Locate and identify every blood parasite.
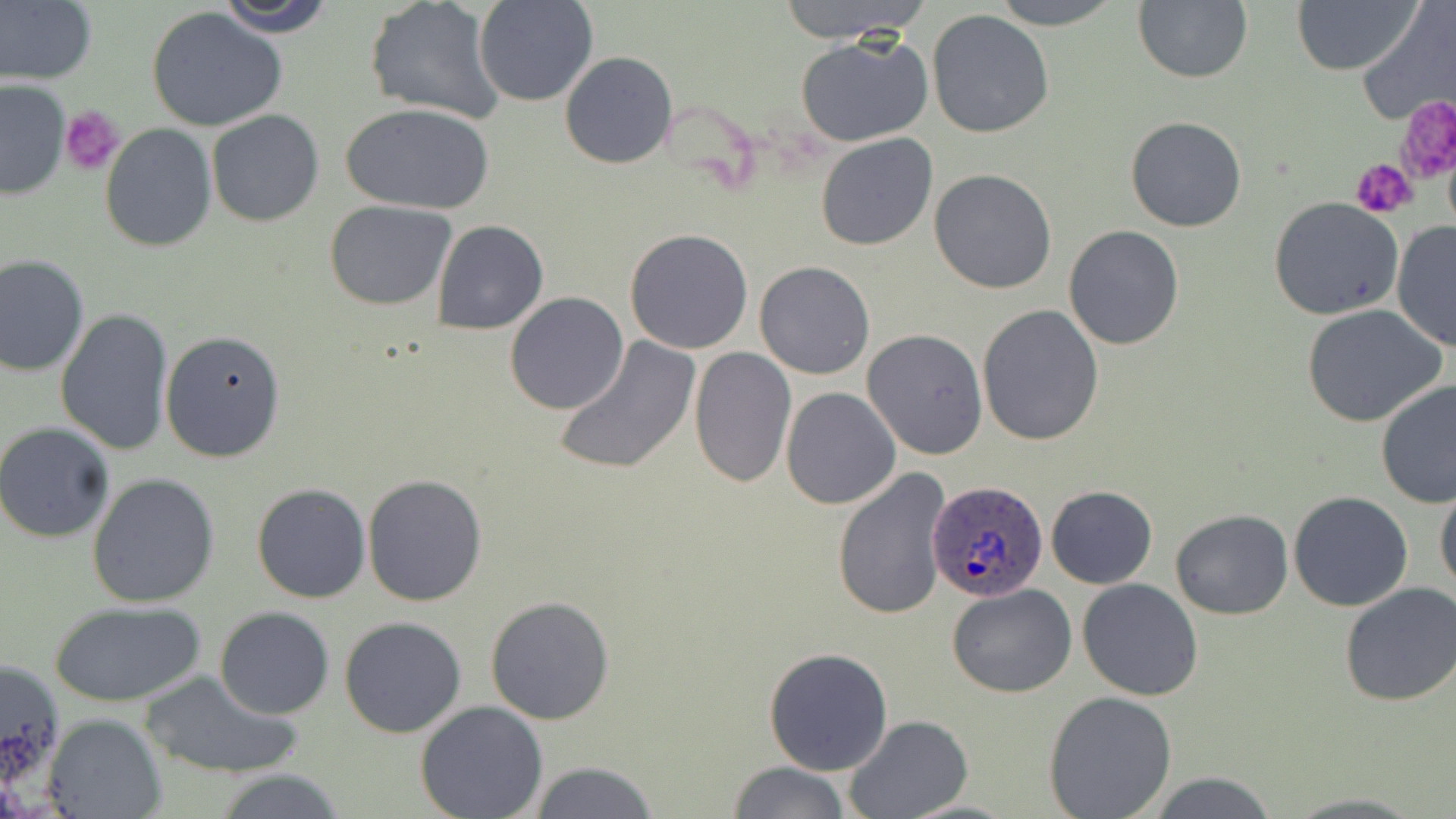

Approximate bounding boxes as named x1/y1/x2/y2 corners in pixels.
Plasmodium ovale-infected red blood cells: (x1=927, y1=479, x2=1051, y2=604).
No Plasmodium falciparum, Plasmodium malariae, Plasmodium vivax, Babesia divergens, or Trypanosoma brucei observed.

Platelet locations: (x1=1397, y1=96, x2=1456, y2=186), (x1=60, y1=106, x2=125, y2=176), (x1=1353, y1=159, x2=1416, y2=219). Uninfected red blood cell locations: (x1=215, y1=0, x2=338, y2=37), (x1=473, y1=0, x2=598, y2=106), (x1=774, y1=0, x2=929, y2=43), (x1=988, y1=0, x2=1125, y2=29), (x1=1134, y1=0, x2=1253, y2=84), (x1=1293, y1=0, x2=1417, y2=75), (x1=365, y1=1, x2=507, y2=126), (x1=0, y1=2, x2=96, y2=84), (x1=1356, y1=2, x2=1456, y2=128), (x1=147, y1=7, x2=289, y2=133), (x1=927, y1=9, x2=1055, y2=138), (x1=796, y1=36, x2=933, y2=147), (x1=560, y1=52, x2=677, y2=170), (x1=0, y1=80, x2=71, y2=199), (x1=340, y1=101, x2=495, y2=215), (x1=206, y1=110, x2=324, y2=227), (x1=1124, y1=115, x2=1247, y2=232), (x1=100, y1=124, x2=217, y2=251), (x1=815, y1=132, x2=938, y2=250), (x1=929, y1=170, x2=1058, y2=294), (x1=1267, y1=197, x2=1405, y2=319), (x1=324, y1=199, x2=457, y2=311), (x1=1392, y1=218, x2=1456, y2=352), (x1=430, y1=220, x2=548, y2=336), (x1=1063, y1=225, x2=1183, y2=351), (x1=624, y1=228, x2=754, y2=355), (x1=0, y1=253, x2=90, y2=376), (x1=754, y1=261, x2=876, y2=380), (x1=505, y1=292, x2=628, y2=414), (x1=977, y1=303, x2=1105, y2=446), (x1=1301, y1=303, x2=1447, y2=427), (x1=55, y1=307, x2=173, y2=457), (x1=159, y1=329, x2=286, y2=462), (x1=863, y1=329, x2=989, y2=458), (x1=553, y1=337, x2=701, y2=477), (x1=688, y1=346, x2=796, y2=489), (x1=1376, y1=379, x2=1456, y2=508), (x1=780, y1=386, x2=901, y2=509), (x1=0, y1=423, x2=115, y2=542), (x1=832, y1=468, x2=953, y2=622), (x1=88, y1=474, x2=220, y2=609), (x1=362, y1=475, x2=488, y2=606), (x1=1433, y1=480, x2=1456, y2=596), (x1=252, y1=483, x2=372, y2=603), (x1=1044, y1=485, x2=1158, y2=589), (x1=1288, y1=491, x2=1415, y2=612), (x1=1171, y1=508, x2=1293, y2=620), (x1=1076, y1=578, x2=1203, y2=701), (x1=1340, y1=581, x2=1456, y2=707), (x1=947, y1=584, x2=1077, y2=697), (x1=484, y1=595, x2=615, y2=725), (x1=51, y1=603, x2=201, y2=708), (x1=214, y1=607, x2=335, y2=719), (x1=338, y1=616, x2=467, y2=739), (x1=764, y1=647, x2=893, y2=775), (x1=0, y1=657, x2=68, y2=797), (x1=138, y1=669, x2=305, y2=780), (x1=1043, y1=691, x2=1178, y2=818), (x1=415, y1=701, x2=549, y2=819), (x1=41, y1=714, x2=165, y2=819), (x1=844, y1=716, x2=970, y2=819), (x1=527, y1=761, x2=662, y2=818), (x1=726, y1=761, x2=851, y2=818), (x1=214, y1=771, x2=346, y2=818), (x1=1145, y1=774, x2=1278, y2=817), (x1=1282, y1=791, x2=1426, y2=817). Slide-level diagnosis: Plasmodium ovale. Optical microscopy. Single field of view. Thin blood smear. May-Grünwald-Giemsa-stained preparation. Image is 1456×819 pixels. Captured at 1000x magnification.